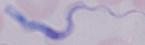

Summary:
  - Modality: micrograph
  - Magnification: 1000x
  - Identification: trypanosome